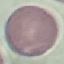 Result: no malaria parasites detected. Automatically extracted cell patch, resized to 64 × 64 pixels. Thin blood film. Photographed with a smartphone camera at the microscope eyepiece. Giemsa stain.